Comment on the morphology of the erythrocytes.
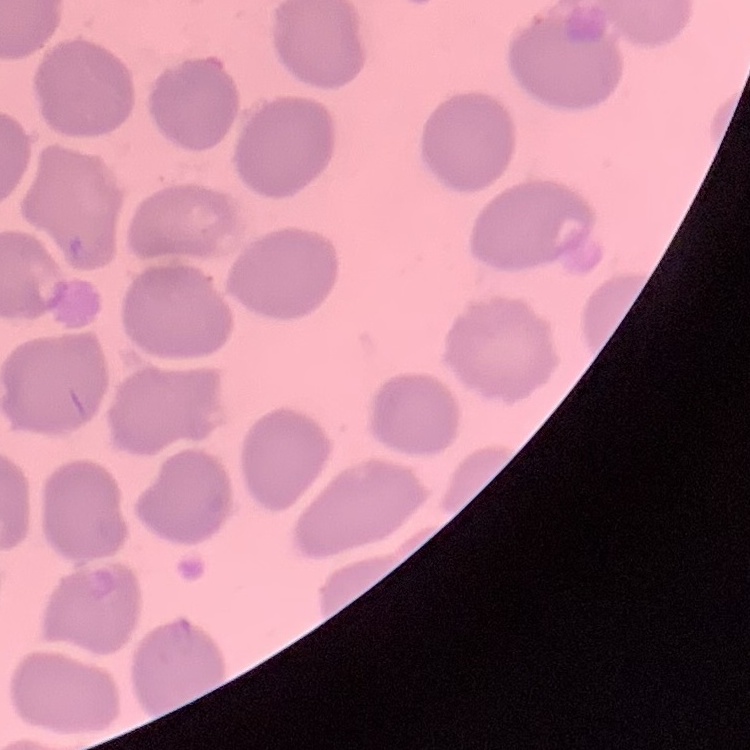
They show no rouleaux formation.

preparation: thin blood smear
image_type: one tile cut from a larger photomicrograph
stain: Field's or Giemsa